Point out each malaria parasite.
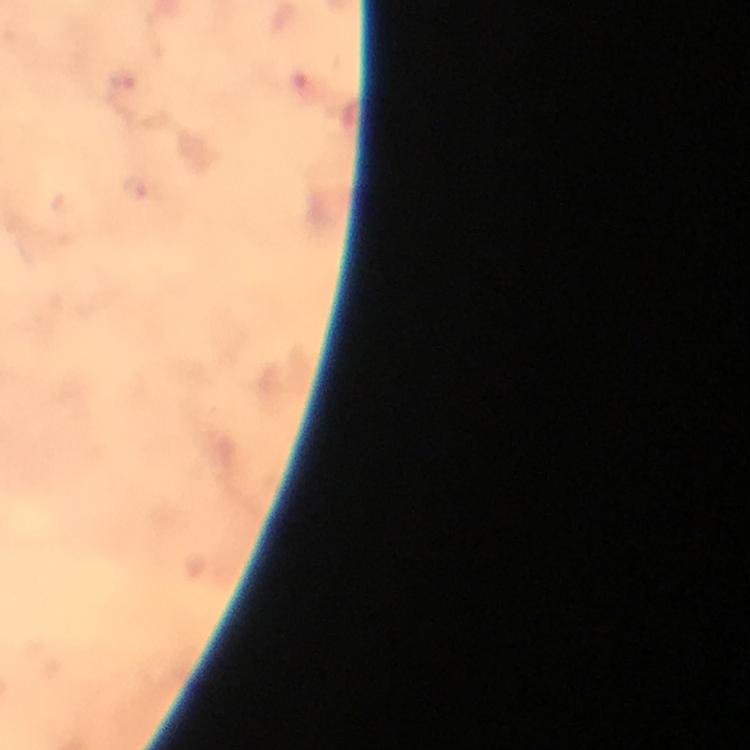
Approximate object centers, in pixels from the top-left corner.
Malaria parasites: (x=135, y=190).

Photographed through the microscope with a smartphone camera. Thick blood smear. Cropped region of a single field of view. From a malaria diagnostic workup. At 100x magnification. Image is 750×750 pixels. Giemsa-stained preparation. Immersion oil was used.